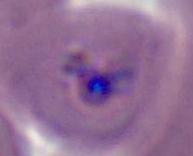 400x or 1000x magnification. A Plasmodium parasite is seen. Micrograph.